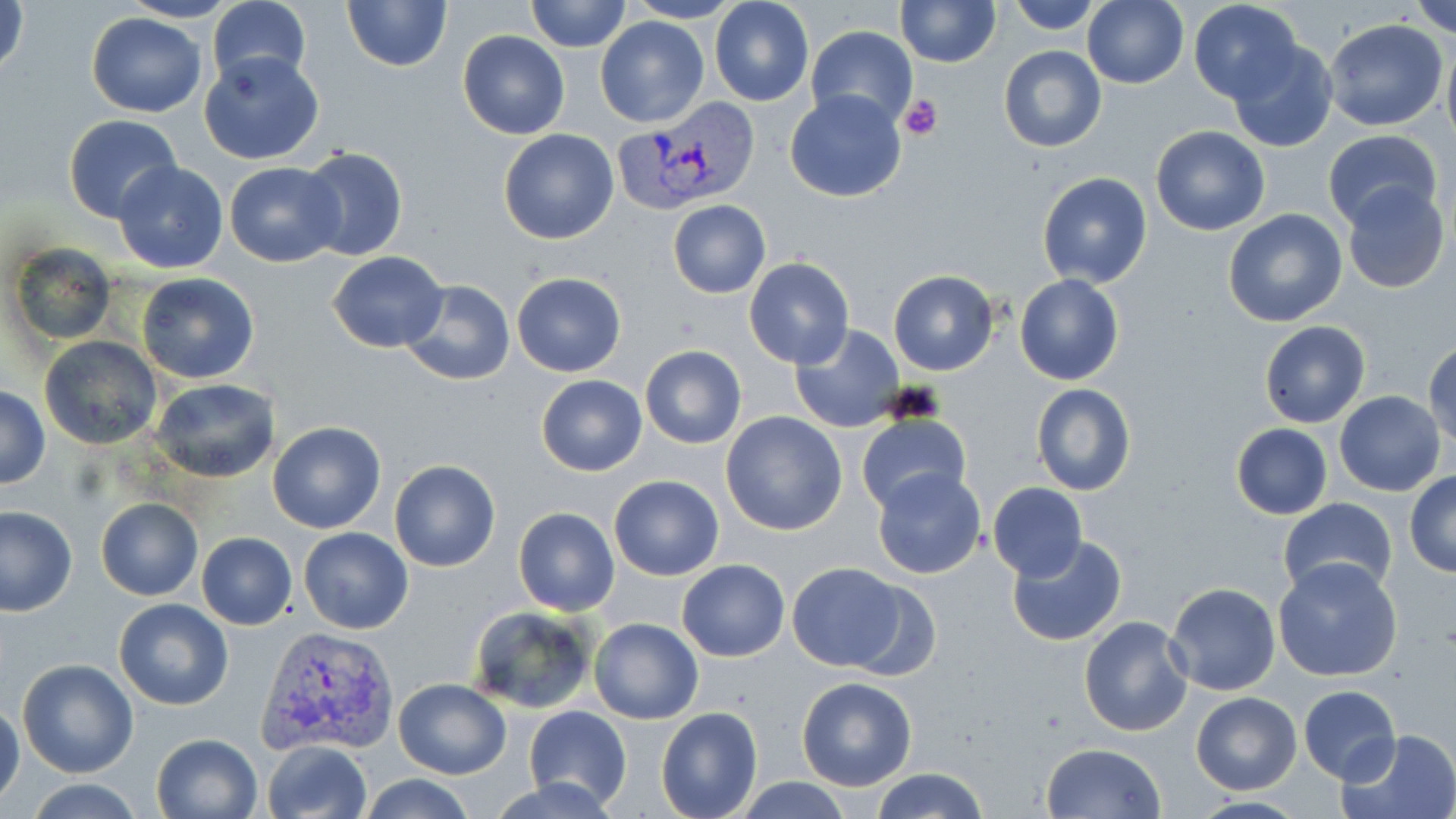

slide-level diagnosis = Plasmodium vivax
preparation = thin blood smear
stain = May-Grünwald-Giemsa
magnification = 1000x
uninfected red blood cell locations = approximate bounding boxes as (x1, y1, x2, y2) in pixels: (1, 0, 30, 83), (116, 0, 242, 23), (207, 0, 312, 91), (340, 0, 452, 72), (527, 0, 631, 51), (624, 0, 746, 24), (709, 0, 815, 106), (896, 0, 1000, 67), (1006, 0, 1106, 33), (1084, 0, 1188, 89), (1188, 0, 1305, 105), (1409, 0, 1456, 36), (85, 11, 206, 118), (593, 15, 710, 127), (1323, 20, 1449, 133), (807, 26, 918, 130), (457, 31, 569, 140), (1226, 37, 1338, 153), (1441, 41, 1456, 151), (998, 45, 1106, 152), (198, 50, 326, 165), (785, 89, 906, 203), (63, 115, 182, 223), (1150, 125, 1271, 236), (497, 129, 618, 244), (1320, 129, 1444, 231), (298, 146, 409, 264), (112, 160, 229, 274), (225, 163, 346, 267), (1036, 171, 1154, 288), (1340, 181, 1450, 295), (666, 199, 772, 299), (1223, 209, 1348, 329), (9, 244, 117, 348), (327, 251, 448, 351), (744, 258, 854, 370), (887, 270, 999, 376), (137, 272, 258, 383), (511, 272, 626, 377), (1015, 274, 1124, 386), (398, 278, 516, 386), (1259, 321, 1370, 428), (790, 324, 904, 432), (39, 337, 164, 452), (1425, 342, 1456, 452), (640, 345, 747, 448), (535, 375, 648, 476), (151, 378, 278, 483), (1029, 383, 1139, 497), (1, 386, 49, 489), (1334, 392, 1445, 495), (721, 411, 849, 536), (856, 414, 971, 516), (267, 422, 387, 535), (1230, 423, 1334, 519), (389, 460, 500, 573), (871, 468, 986, 580), (1404, 471, 1456, 576), (608, 473, 724, 581), (987, 483, 1087, 581), (1278, 497, 1398, 596), (96, 498, 202, 601), (0, 505, 77, 616), (513, 507, 619, 615), (299, 527, 412, 634), (196, 532, 298, 629), (1005, 535, 1128, 647), (1272, 557, 1404, 682), (677, 559, 790, 662), (786, 562, 909, 671), (840, 578, 944, 679), (1166, 582, 1281, 696), (114, 598, 234, 711), (466, 605, 598, 714), (1078, 615, 1192, 737), (590, 618, 704, 724), (17, 658, 139, 778), (796, 677, 917, 791), (392, 679, 510, 779), (1298, 685, 1401, 784), (1190, 690, 1303, 795), (0, 701, 25, 809), (524, 706, 631, 811), (655, 708, 764, 819), (1338, 728, 1456, 819), (150, 733, 262, 819), (263, 740, 372, 819), (1041, 742, 1166, 819), (870, 767, 988, 819), (359, 775, 475, 819), (488, 775, 625, 818), (731, 777, 854, 817), (19, 778, 151, 818)
field of view = single
image size = 1456×819 pixels
modality = light microscopy
platelet locations = approximate bounding boxes as (x1, y1, x2, y2) in pixels: (900, 95, 943, 140)
Plasmodium vivax-infected red blood cell locations = approximate bounding boxes as (x1, y1, x2, y2) in pixels: (614, 103, 758, 214), (256, 627, 400, 759)